Identify the blood parasite species.
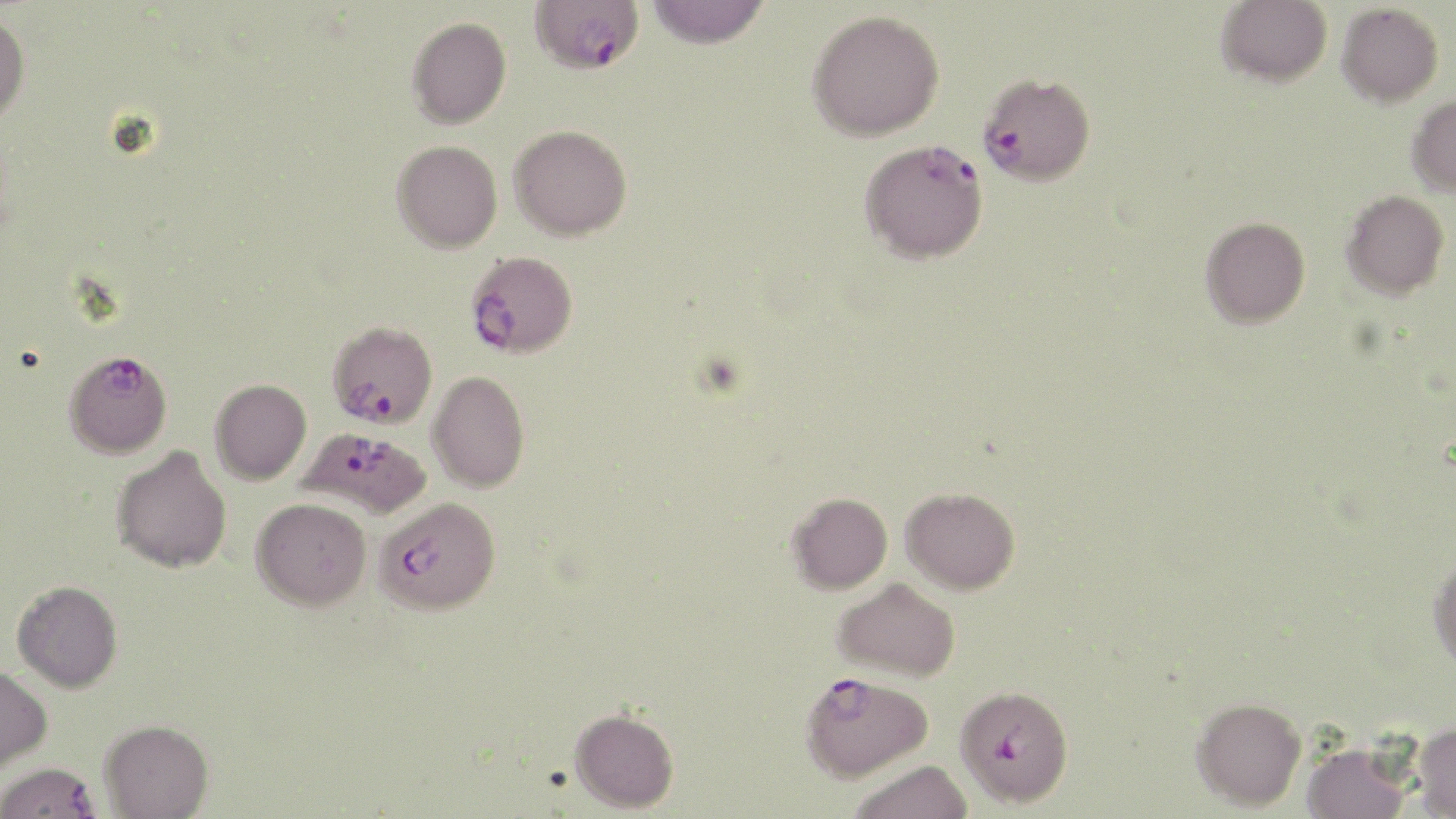
Plasmodium falciparum.

Approximate bounding boxes as (x1, y1, x2, y2) in pixels. Uninfected red blood cell locations (subset): (645, 0, 770, 48), (1216, 0, 1332, 87), (1337, 2, 1444, 107), (807, 9, 944, 141), (0, 11, 30, 128), (407, 16, 511, 129), (1407, 94, 1456, 196), (509, 124, 632, 241), (392, 140, 502, 252), (1341, 190, 1449, 299), (1200, 216, 1310, 328), (427, 370, 530, 492), (210, 379, 312, 484), (111, 444, 232, 573), (901, 487, 1020, 594), (788, 493, 892, 594), (251, 497, 372, 611), (1428, 555, 1456, 672), (833, 578, 960, 681), (12, 580, 122, 692), (0, 665, 52, 772), (1191, 697, 1306, 811), (569, 707, 679, 812), (100, 719, 213, 818), (1412, 722, 1456, 818), (1301, 740, 1412, 819), (848, 759, 974, 819). Plasmodium falciparum-infected red blood cell locations (subset): (530, 0, 644, 75), (978, 73, 1096, 186), (859, 138, 988, 264), (465, 251, 578, 358), (326, 320, 437, 429), (64, 349, 172, 458), (296, 427, 431, 519), (374, 497, 500, 615), (800, 671, 933, 780), (0, 762, 101, 819). One field of a larger specimen. Captured at 1000x magnification. May-Grünwald-Giemsa stain. Optical microscopy. Thin blood film. Image is 1456×819 pixels.